Point out each malaria parasite and each leukocyte.
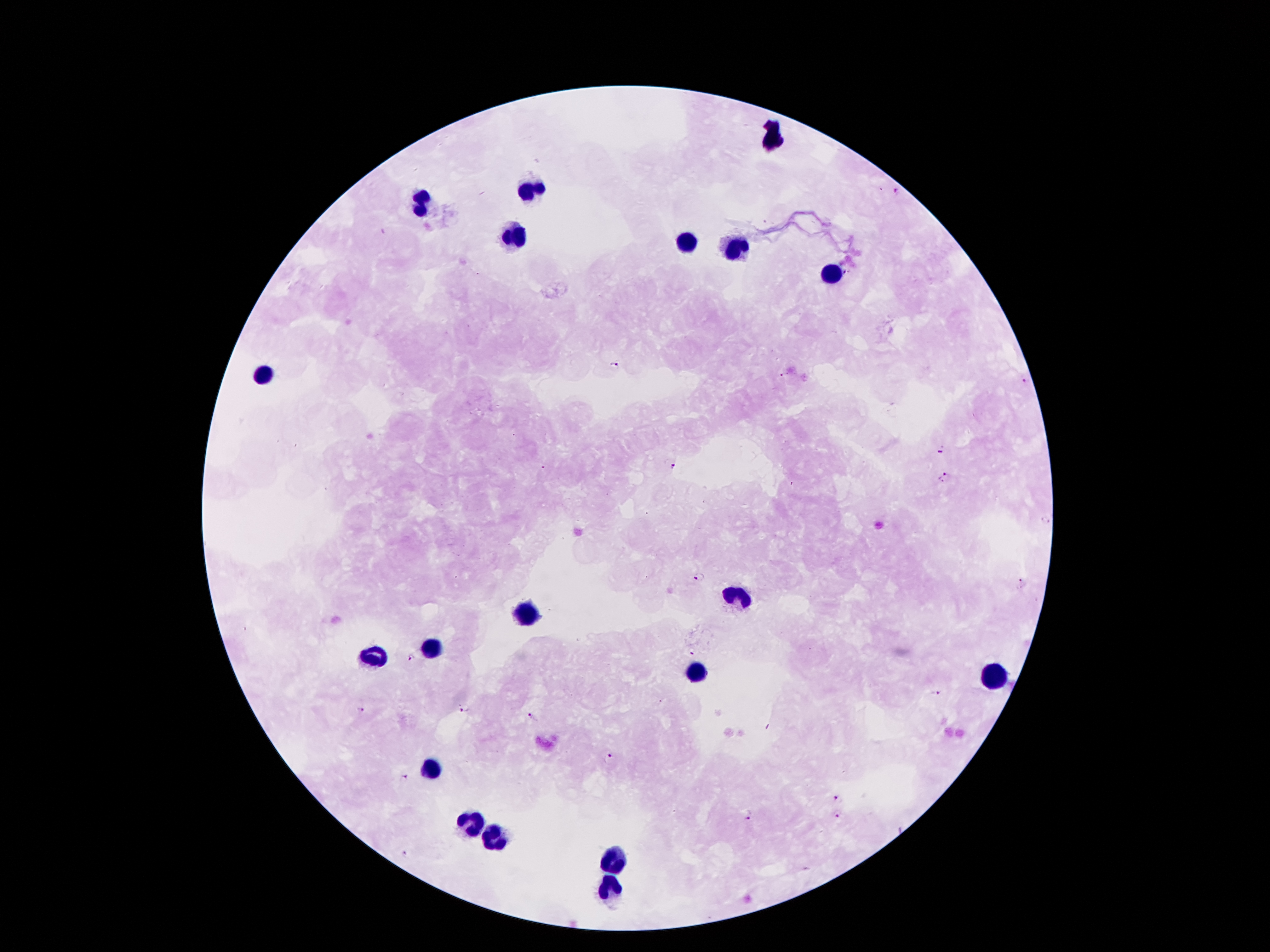
Approximate object centers, in pixels from the top-left corner.
Malaria parasites: (x=898, y=193), (x=615, y=365), (x=1026, y=379), (x=941, y=449), (x=670, y=465), (x=944, y=478), (x=1044, y=522), (x=698, y=576), (x=1020, y=584), (x=691, y=655), (x=410, y=658), (x=934, y=694), (x=466, y=707), (x=361, y=709), (x=531, y=716), (x=608, y=756), (x=404, y=779), (x=839, y=799), (x=837, y=813), (x=747, y=816), (x=404, y=855).
Leukocytes: (x=528, y=195), (x=425, y=205), (x=514, y=235), (x=690, y=246), (x=738, y=250), (x=831, y=275), (x=267, y=372), (x=736, y=596), (x=525, y=615), (x=432, y=650), (x=375, y=656), (x=700, y=674), (x=991, y=677), (x=430, y=769), (x=468, y=822), (x=494, y=839), (x=611, y=859), (x=611, y=886).

patient malaria status = positive for Plasmodium falciparum
preparation = thick blood film
image size = 1270×952 pixels
capture = smartphone through the microscope eyepiece
field of view = one from this slide
magnification = 100x
stain = Giemsa